Classify this cell by malaria status.
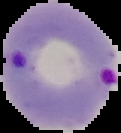
It is parasitized.

Summary:
  - Preparation: thin blood smear
  - Image size: 121×133 pixels
  - Image type: segmented cell region with the area outside set to black